Identify the parasite.
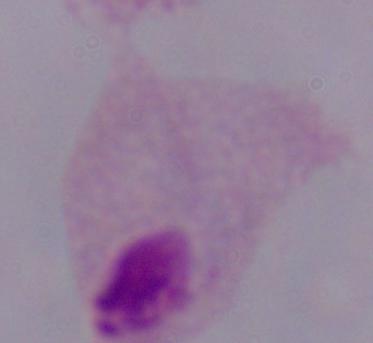
A trichomonad.

Summary:
  - Magnification: 1000x
  - Modality: photomicrograph